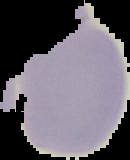

Summary:
  - Image type: cell region segmented out of the field of view; surrounding area masked to black
  - Result: negative for Plasmodium parasites
  - Image size: 130×160 pixels
  - Preparation: thin blood smear